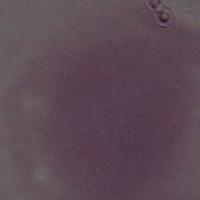

{
  "magnification": "1000x",
  "modality": "micrograph",
  "identification": "red blood cell"
}